State which cell type is depicted.
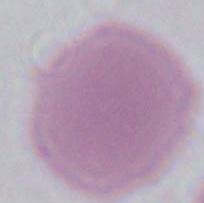
An erythrocyte.

{
  "magnification": "1000x",
  "modality": "photomicrograph"
}